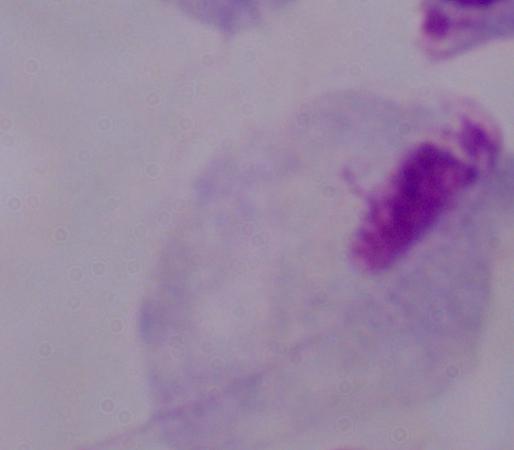 Photomicrograph. Captured at 1000x magnification. A trichomonad is seen.